Name the blood parasite species.
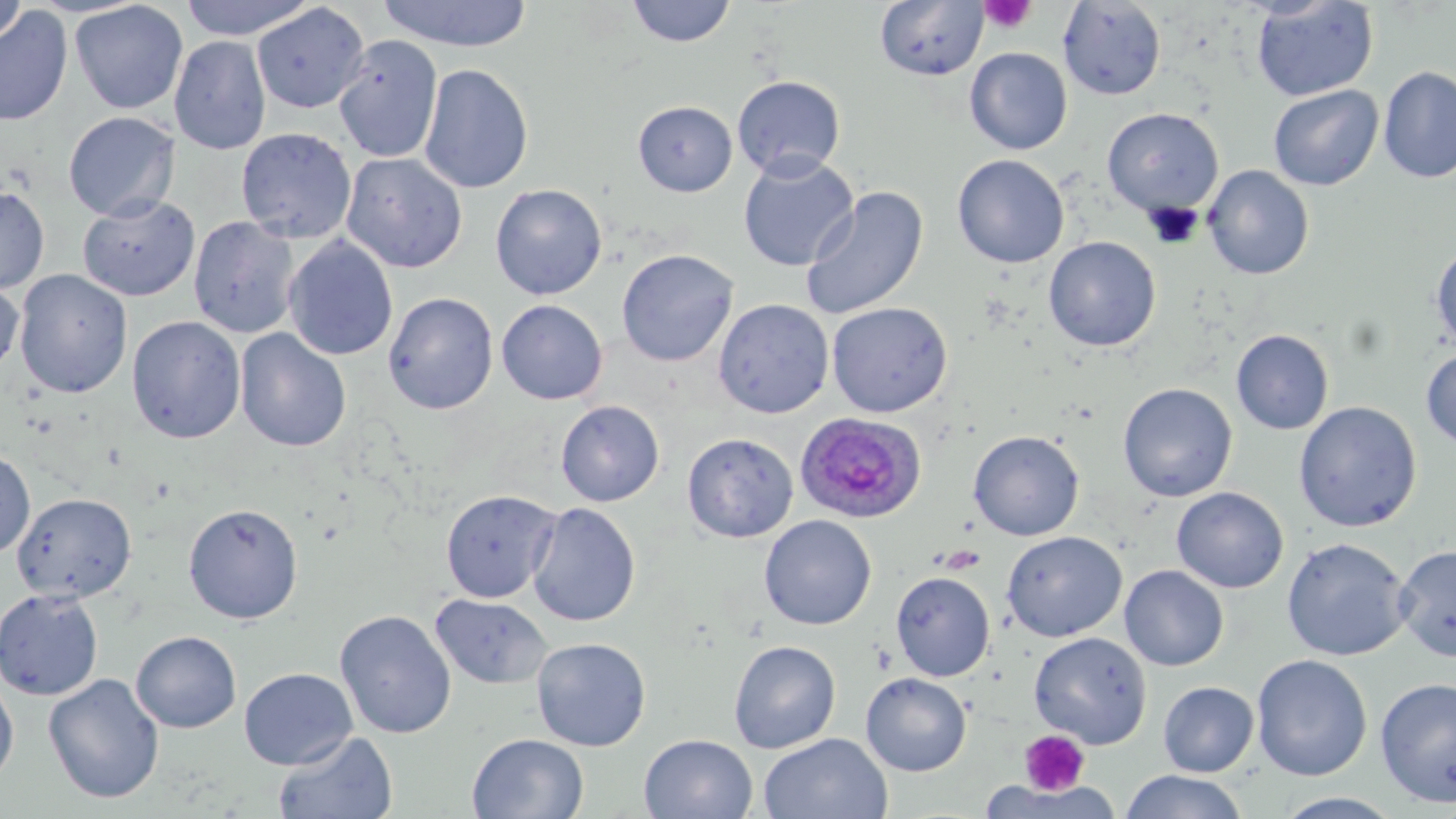
Plasmodium ovale.

{
  "platelet_locations": "approximate bounding boxes as (x1,y1)-(x2,y2) corner pairs in pixels: (979,1)-(1036,34), (1019,730)-(1090,796)",
  "uninfected_red_blood_cell_locations": "approximate bounding boxes as (x1,y1)-(x2,y2) corner pairs in pixels: (178,0)-(320,40), (376,0)-(534,52), (626,0)-(736,48), (0,1)-(29,48), (70,1)-(188,114), (1058,1)-(1166,100), (1251,1)-(1379,102), (875,2)-(989,81), (251,3)-(369,114), (0,7)-(73,126), (169,35)-(272,155), (333,35)-(443,163), (964,48)-(1072,155), (419,63)-(534,194), (1378,66)-(1456,183), (732,75)-(846,180), (1268,85)-(1383,191), (633,100)-(737,196), (1102,107)-(1223,217), (63,111)-(180,221), (236,127)-(357,244), (341,152)-(468,273), (738,153)-(859,272), (952,154)-(1069,268), (1203,165)-(1314,280), (490,183)-(608,300), (800,185)-(928,320), (0,186)-(49,294), (78,194)-(199,301), (188,215)-(300,339), (283,236)-(398,361), (1044,237)-(1161,352), (1430,241)-(1456,352), (616,249)-(739,367), (14,269)-(133,399), (0,278)-(24,380), (384,292)-(498,415), (496,299)-(608,405), (713,299)-(834,419), (827,301)-(952,417), (127,315)-(246,444), (236,329)-(351,452), (1231,329)-(1334,434), (1420,346)-(1456,452), (1117,383)-(1238,502), (556,400)-(664,507), (1294,401)-(1422,532), (968,431)-(1084,541), (682,433)-(798,543), (0,449)-(35,559), (1172,487)-(1288,593), (441,490)-(560,603), (12,492)-(136,602), (183,503)-(303,624), (527,503)-(640,627), (758,515)-(877,630), (1002,531)-(1126,641), (1281,537)-(1411,661), (1393,544)-(1456,663), (1119,565)-(1229,671), (890,571)-(995,681), (879,573)-(985,776), (0,588)-(104,701), (430,593)-(552,690), (334,609)-(457,739), (131,631)-(242,732), (1029,631)-(1151,748), (531,637)-(651,751), (728,640)-(841,753), (1251,654)-(1372,781), (238,667)-(358,770), (0,673)-(19,786), (43,673)-(165,804), (860,673)-(971,776), (1375,676)-(1456,807), (1158,681)-(1259,777), (273,730)-(398,819), (467,733)-(589,819), (759,733)-(893,819), (639,734)-(758,819), (1120,770)-(1249,819), (979,780)-(1126,819), (1273,791)-(1405,818)",
  "image_size": "1456×819 pixels",
  "preparation": "thin blood smear",
  "field_of_view": "single",
  "stain": "May-Grünwald-Giemsa",
  "plasmodium_ovale_infected_red_blood_cell_locations": "approximate bounding boxes as (x1,y1)-(x2,y2) corner pairs in pixels: (796,412)-(927,523)",
  "magnification": "1000x",
  "modality": "optical microscopy"
}